Locate and identify every blood parasite.
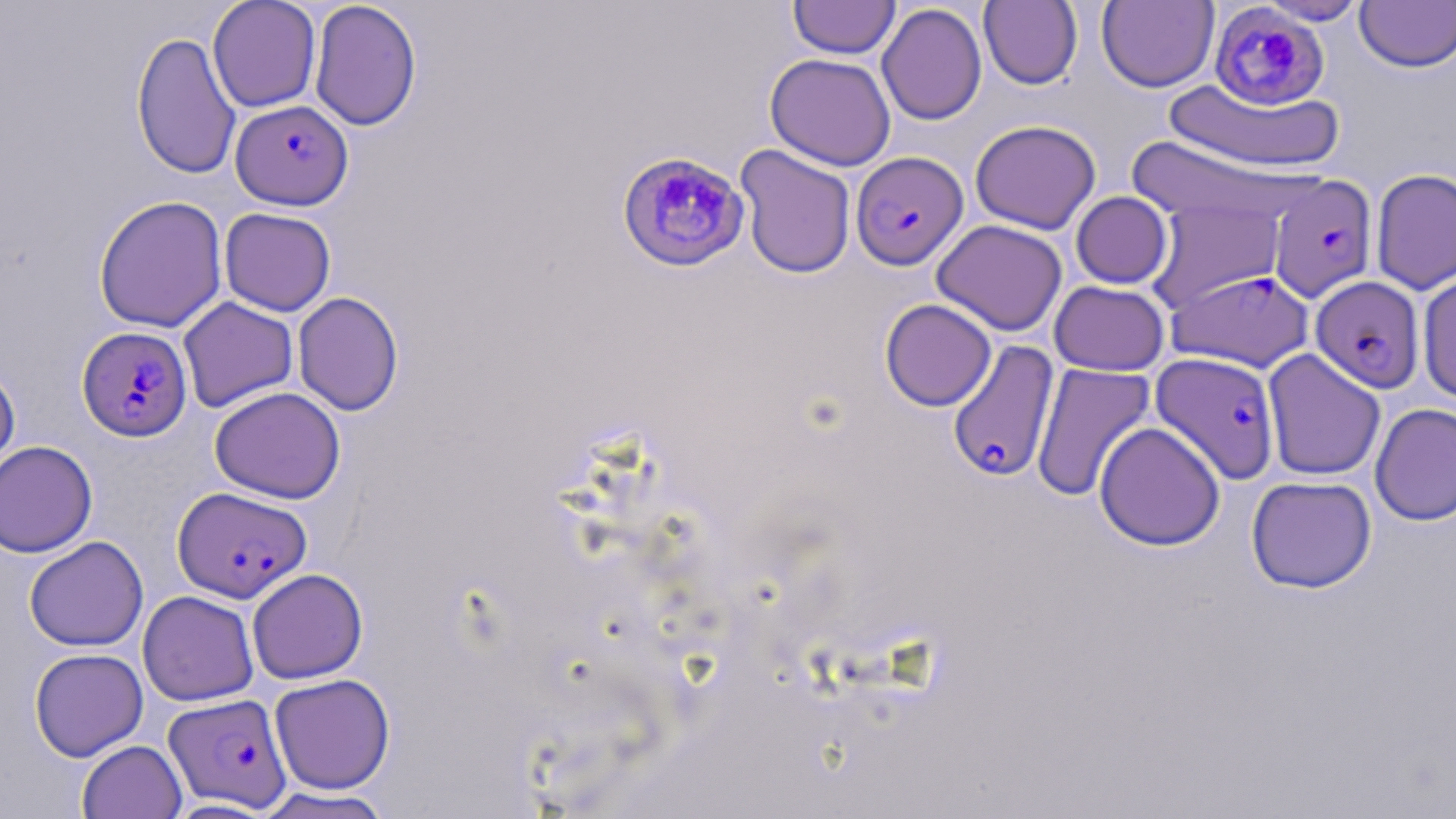
Approximate bounding boxes as [x1, y1, x2, y2] in pixels.
Plasmodium falciparum-infected red blood cells: [1209, 3, 1329, 111], [229, 99, 353, 210], [616, 151, 750, 272], [850, 152, 969, 270], [1268, 175, 1377, 302], [1167, 269, 1314, 372], [1311, 276, 1425, 393], [77, 326, 193, 442], [947, 340, 1060, 483], [1150, 353, 1281, 484], [172, 486, 312, 603], [163, 693, 291, 811].
No Plasmodium ovale, Plasmodium malariae, Plasmodium vivax, Babesia divergens, or Trypanosoma brucei observed.

slide-level diagnosis = Plasmodium falciparum
magnification = 1000x
uninfected red blood cell locations = approximate bounding boxes as [x1, y1, x2, y2] in pixels: [207, 0, 321, 112], [789, 0, 900, 59], [979, 0, 1082, 90], [1097, 0, 1218, 92], [1256, 0, 1369, 25], [1355, 0, 1456, 73], [309, 1, 422, 132], [876, 3, 987, 126], [131, 30, 241, 179], [765, 53, 896, 171], [1163, 78, 1344, 173], [970, 119, 1101, 235], [1120, 135, 1307, 223], [735, 144, 857, 278], [1371, 168, 1456, 294], [1071, 191, 1173, 289], [93, 195, 228, 332], [1145, 199, 1285, 313], [219, 208, 336, 316], [931, 219, 1067, 336], [1417, 270, 1456, 403], [1049, 281, 1170, 376], [292, 291, 404, 416], [178, 296, 299, 413], [879, 298, 996, 411], [1262, 348, 1386, 481], [1030, 362, 1156, 502], [0, 365, 20, 488], [209, 386, 346, 504], [1370, 403, 1456, 526], [1094, 422, 1225, 551], [0, 441, 98, 557], [1246, 476, 1377, 594], [24, 536, 148, 652], [247, 568, 368, 684], [137, 590, 259, 706], [29, 647, 148, 761], [269, 673, 396, 794], [77, 739, 187, 818], [254, 787, 396, 818], [163, 799, 280, 818]
image size = 1456×819 pixels
field of view = one of a larger specimen
modality = light microscopy
preparation = thin blood smear
stain = May-Grünwald-Giemsa